Locate every leukocyte (white blood cell).
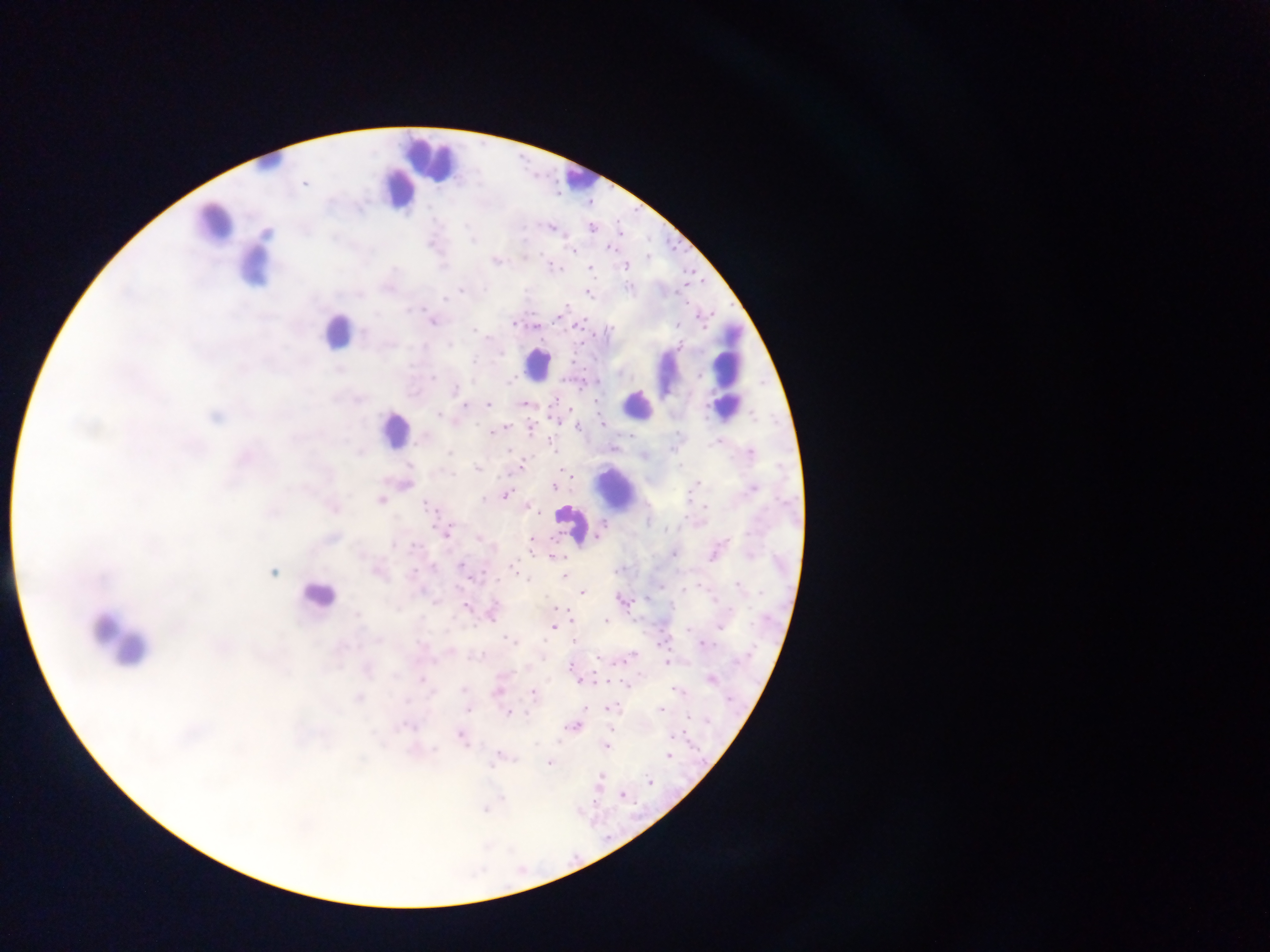
Approximate centers as [x, y] in pixels.
Leukocytes: [428, 160], [267, 164], [578, 179], [399, 188], [214, 224], [253, 264], [337, 331], [537, 364], [725, 369], [637, 404], [393, 430], [615, 487], [572, 524], [318, 596], [119, 642].

{
  "capture": "mobile-phone photograph through a microscope",
  "country": "Ghana",
  "plasmodium_parasite_locations": "approximate centers as [x, y] in pixels: [303, 184], [551, 228], [592, 228], [619, 233], [608, 249], [570, 250], [523, 256], [623, 266], [589, 268], [587, 292], [431, 321], [596, 400], [488, 404], [523, 404], [439, 414], [215, 416], [556, 420], [601, 424], [578, 426], [504, 427], [530, 428], [553, 449], [613, 449], [644, 454], [521, 466], [478, 469], [564, 470], [405, 484], [553, 486], [753, 488], [504, 493], [381, 501], [427, 505], [527, 506], [334, 507], [600, 531], [445, 532], [480, 536], [532, 538], [553, 557], [462, 566], [513, 568], [377, 570], [273, 572], [565, 575], [582, 591], [646, 598], [622, 601], [466, 606], [552, 608], [561, 608], [491, 612], [566, 612], [606, 622], [553, 627], [574, 638], [504, 640], [667, 662], [570, 664], [420, 679], [710, 679], [579, 680], [627, 684], [464, 690], [677, 690], [497, 693], [532, 694], [358, 698], [467, 708], [609, 708], [661, 709], [508, 711], [573, 726], [672, 734], [461, 736], [606, 745], [669, 756], [497, 757], [550, 763], [600, 775], [649, 782], [623, 794], [485, 808]",
  "preparation": "thick blood film",
  "field_of_view": "single",
  "image_size": "1270×952 pixels"
}